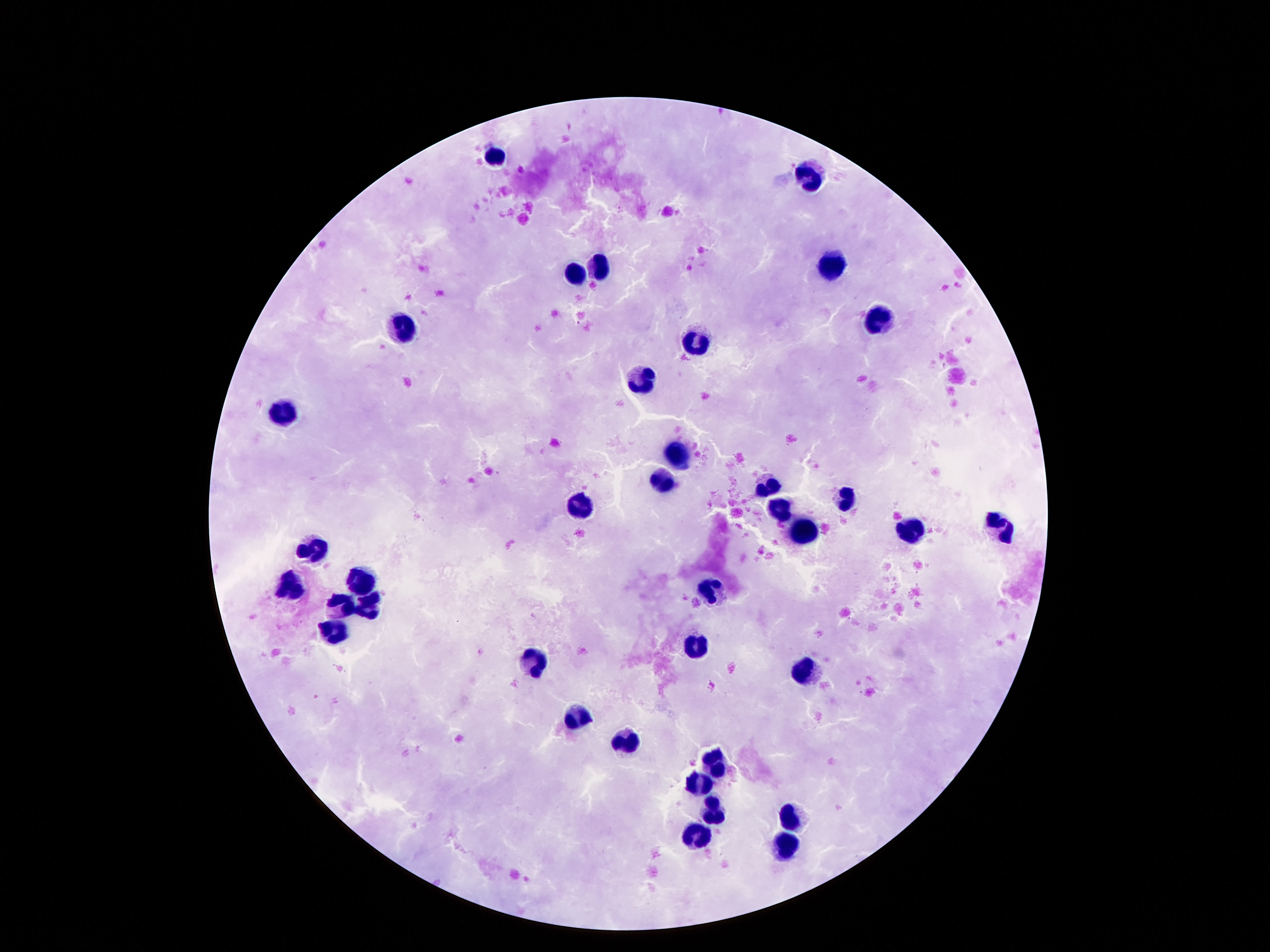

Approximate object centers, in pixels from the top-left corner.
Summary:
  - Leukocyte locations: (x=494, y=155), (x=810, y=173), (x=832, y=265), (x=600, y=269), (x=574, y=271), (x=878, y=318), (x=404, y=324), (x=700, y=339), (x=644, y=379), (x=288, y=414), (x=678, y=453), (x=666, y=482), (x=768, y=487), (x=846, y=499), (x=780, y=507), (x=582, y=508), (x=1002, y=526), (x=906, y=530), (x=802, y=531), (x=316, y=549), (x=360, y=584), (x=288, y=585), (x=714, y=587), (x=342, y=607), (x=370, y=607), (x=336, y=635), (x=694, y=647), (x=536, y=661), (x=806, y=670), (x=578, y=719), (x=624, y=739), (x=718, y=765), (x=698, y=783), (x=714, y=811), (x=792, y=817), (x=700, y=837), (x=784, y=846)
  - Magnification: 100x
  - Preparation: thick blood film
  - Patient malaria status: negative
  - Capture: smartphone camera through the microscope eyepiece
  - Stain: Giemsa
  - Field of view: single
  - Image size: 1270×952 pixels